Assess this cell for malaria.
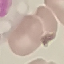

It is uninfected.

image type = cell patch, automatically extracted from a larger field of view and resized to 64 × 64 pixels
preparation = thin blood smear
capture = smartphone camera at the microscope eyepiece
stain = Giemsa